Report the malaria status of this cell.
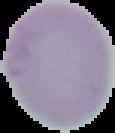

It is uninfected.

{
  "image_size": "115×133 pixels",
  "preparation": "thin blood smear",
  "image_type": "cell region segmented out of the field of view; surrounding area masked to black"
}